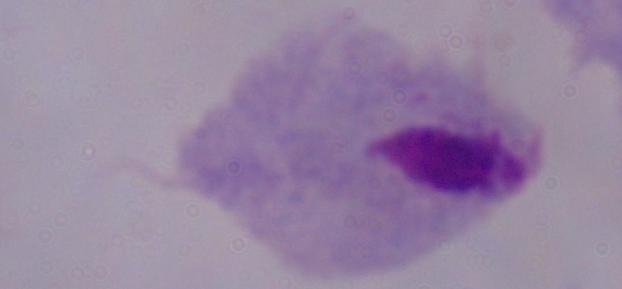

modality = micrograph
magnification = 1000x
identification = trichomonad